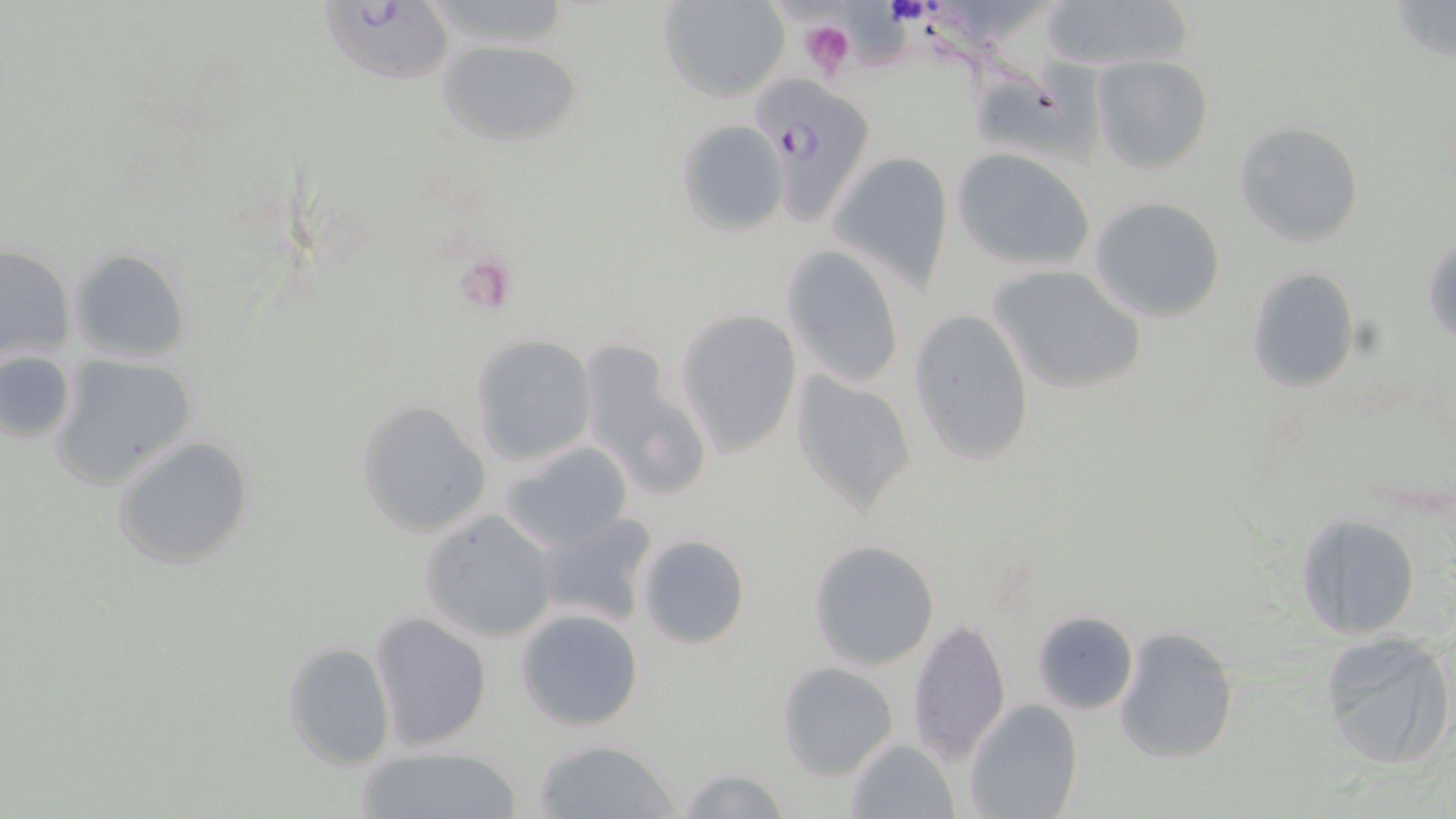

slide-level diagnosis = Plasmodium falciparum
field of view = one of a larger specimen
image size = 1456×819 pixels
Plasmodium falciparum-infected red blood cell locations = approximate bounding boxes as (x1, y1, x2, y2) in pixels: (327, 0, 473, 87), (747, 71, 879, 224)
uninfected red blood cell locations = approximate bounding boxes as (x1, y1, x2, y2) in pixels: (657, 0, 789, 103), (1039, 0, 1193, 73), (1388, 0, 1455, 64), (435, 37, 582, 146), (1093, 56, 1214, 173), (976, 59, 1111, 177), (675, 120, 789, 236), (1234, 122, 1364, 247), (951, 148, 1097, 271), (831, 151, 954, 291), (1088, 198, 1226, 322), (1424, 233, 1455, 346), (0, 245, 73, 366), (782, 245, 907, 388), (69, 248, 191, 364), (989, 263, 1147, 394), (1245, 269, 1360, 391), (676, 308, 804, 458), (908, 309, 1035, 467), (469, 335, 597, 465), (578, 341, 711, 499), (0, 349, 77, 445), (52, 354, 195, 492), (790, 371, 916, 518), (356, 401, 493, 536), (111, 435, 254, 572), (502, 442, 633, 550), (420, 509, 560, 642), (530, 512, 659, 630), (1296, 513, 1421, 640), (635, 534, 752, 649), (808, 540, 940, 670), (515, 607, 644, 731), (1031, 609, 1138, 714), (368, 612, 492, 750), (905, 618, 1010, 765), (1114, 627, 1238, 764), (1317, 633, 1455, 770), (283, 640, 394, 771), (777, 662, 898, 779), (964, 699, 1082, 818), (532, 738, 680, 819), (844, 738, 958, 818), (353, 745, 524, 819), (676, 766, 791, 819)
magnification = 1000x
modality = optical microscopy
preparation = thin blood film
platelet locations = approximate bounding boxes as (x1, y1, x2, y2) in pixels: (883, 0, 930, 27), (798, 17, 858, 80), (464, 264, 525, 311)
stain = May-Grünwald-Giemsa